Classify this cell by malaria status.
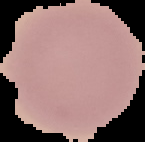

Uninfected.

image size = 145×142 pixels
preparation = thin blood smear
image type = cell region segmented out of the field of view; surrounding area masked to black